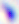
Summary:
  - Identification: Toxoplasma gondii
  - Magnification: 400x
  - Modality: photomicrograph